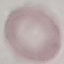
malaria status = uninfected
capture = smartphone camera at the microscope eyepiece
preparation = thin blood film
stain = Giemsa
image type = automatically extracted cell patch, resized to 64 × 64 pixels